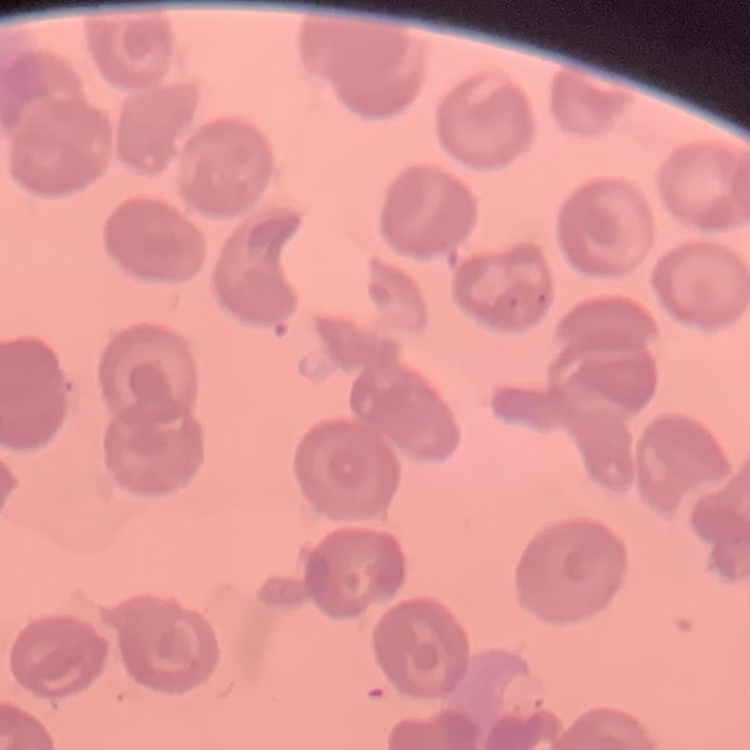

Summary:
  - Erythrocyte morphology: no rouleaux formation
  - Image type: square crop of a larger photomicrograph
  - Stain: Field's or Giemsa
  - Preparation: thin blood film